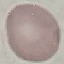
Result: negative for malaria parasites. Automatically extracted cell patch, resized to 64 × 64 pixels. Thin smear of blood. Giemsa-stained preparation. Acquired by smartphone through the microscope eyepiece.